Locate every Plasmodium falciparum-infected red blood cell.
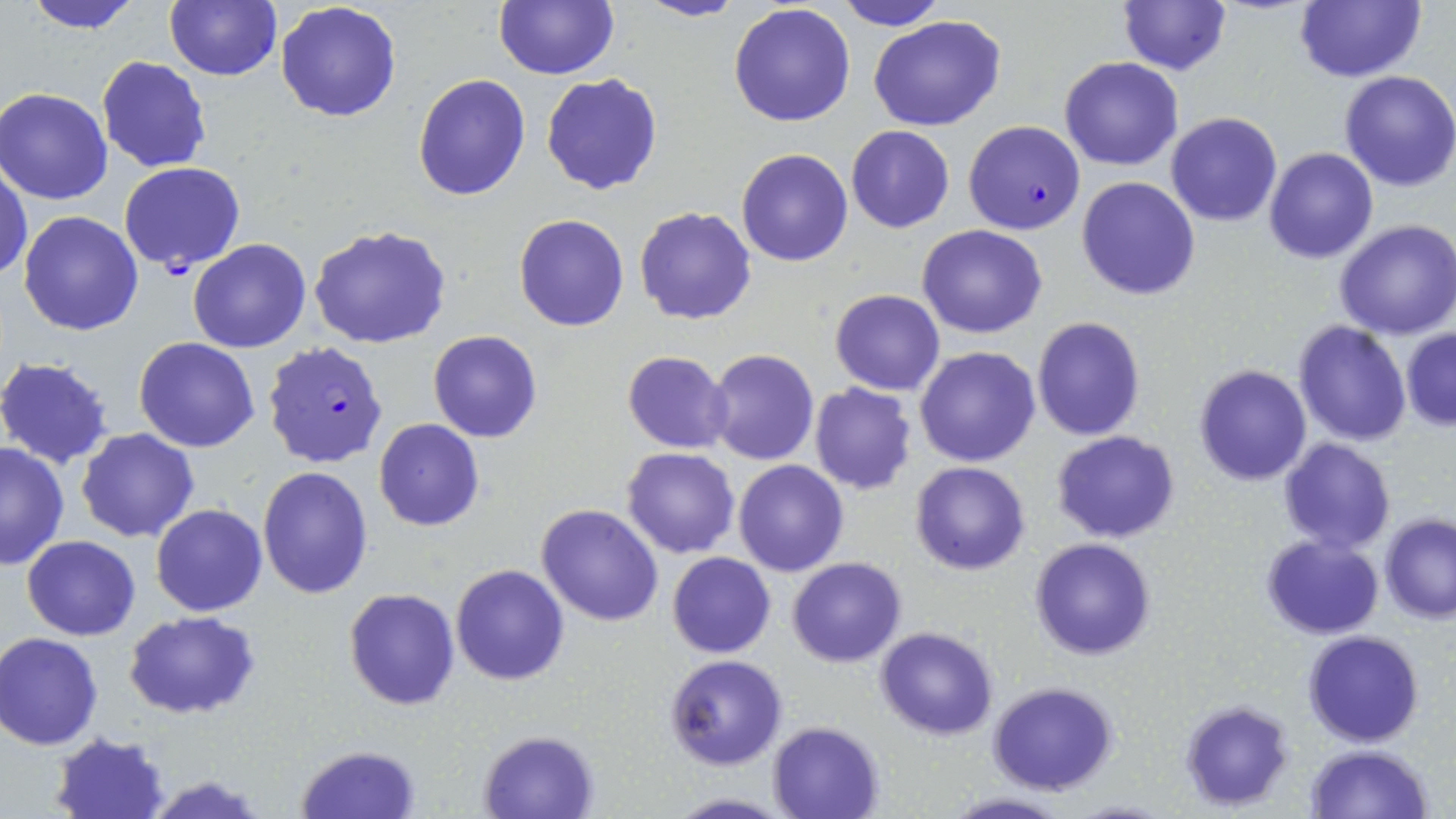
Approximate bounding boxes as [x1, y1, x2, y2] in pixels.
Plasmodium falciparum-infected red blood cells: [963, 120, 1085, 235], [118, 161, 247, 275], [262, 340, 389, 470].

slide-level diagnosis = Plasmodium falciparum
preparation = thin blood film
stain = May-Grünwald-Giemsa
field of view = one of a larger specimen
magnification = 1000x
image size = 1456×819 pixels
uninfected red blood cell locations = approximate bounding boxes as [x1, y1, x2, y2] in pixels: [21, 0, 147, 34], [164, 0, 282, 82], [495, 0, 618, 80], [635, 0, 744, 23], [834, 0, 947, 30], [1294, 0, 1424, 84], [275, 1, 401, 121], [1116, 1, 1231, 76], [728, 4, 857, 127], [867, 16, 1007, 132], [96, 56, 212, 172], [1060, 57, 1182, 170], [1338, 70, 1456, 193], [540, 71, 664, 196], [412, 74, 531, 201], [1, 88, 115, 204], [1166, 112, 1282, 226], [845, 125, 954, 233], [736, 147, 854, 267], [1263, 147, 1378, 264], [0, 159, 32, 282], [1076, 176, 1200, 300], [634, 205, 758, 325], [19, 211, 144, 335], [513, 213, 629, 331], [1334, 218, 1456, 339], [916, 223, 1048, 340], [310, 224, 451, 351], [187, 238, 311, 352], [829, 288, 944, 394], [1031, 316, 1146, 440], [1292, 320, 1412, 447], [1400, 327, 1456, 431], [427, 330, 542, 443], [134, 338, 261, 453], [914, 346, 1040, 467], [703, 348, 819, 466], [621, 351, 735, 454], [0, 356, 116, 467], [1192, 363, 1312, 486], [807, 382, 918, 495], [374, 418, 485, 531], [77, 428, 199, 544], [1052, 430, 1180, 543], [1278, 438, 1395, 553], [0, 442, 69, 571], [622, 447, 741, 559], [734, 459, 849, 577], [908, 461, 1031, 576], [257, 466, 373, 597], [536, 503, 664, 625], [152, 504, 268, 617], [1380, 513, 1456, 622], [1260, 534, 1384, 639], [23, 535, 140, 639], [1030, 537, 1157, 660], [666, 552, 777, 659], [788, 557, 906, 667], [449, 563, 569, 686], [344, 588, 460, 710], [122, 611, 262, 718], [875, 626, 999, 740], [1303, 630, 1423, 747], [0, 633, 104, 749], [663, 654, 788, 772], [987, 682, 1121, 796], [1178, 700, 1294, 810], [768, 721, 884, 819], [479, 729, 600, 818], [51, 731, 171, 818], [296, 744, 419, 818], [1305, 744, 1435, 819], [146, 774, 270, 818], [940, 791, 1074, 819], [661, 792, 794, 819], [1062, 799, 1179, 818]
modality = optical microscopy